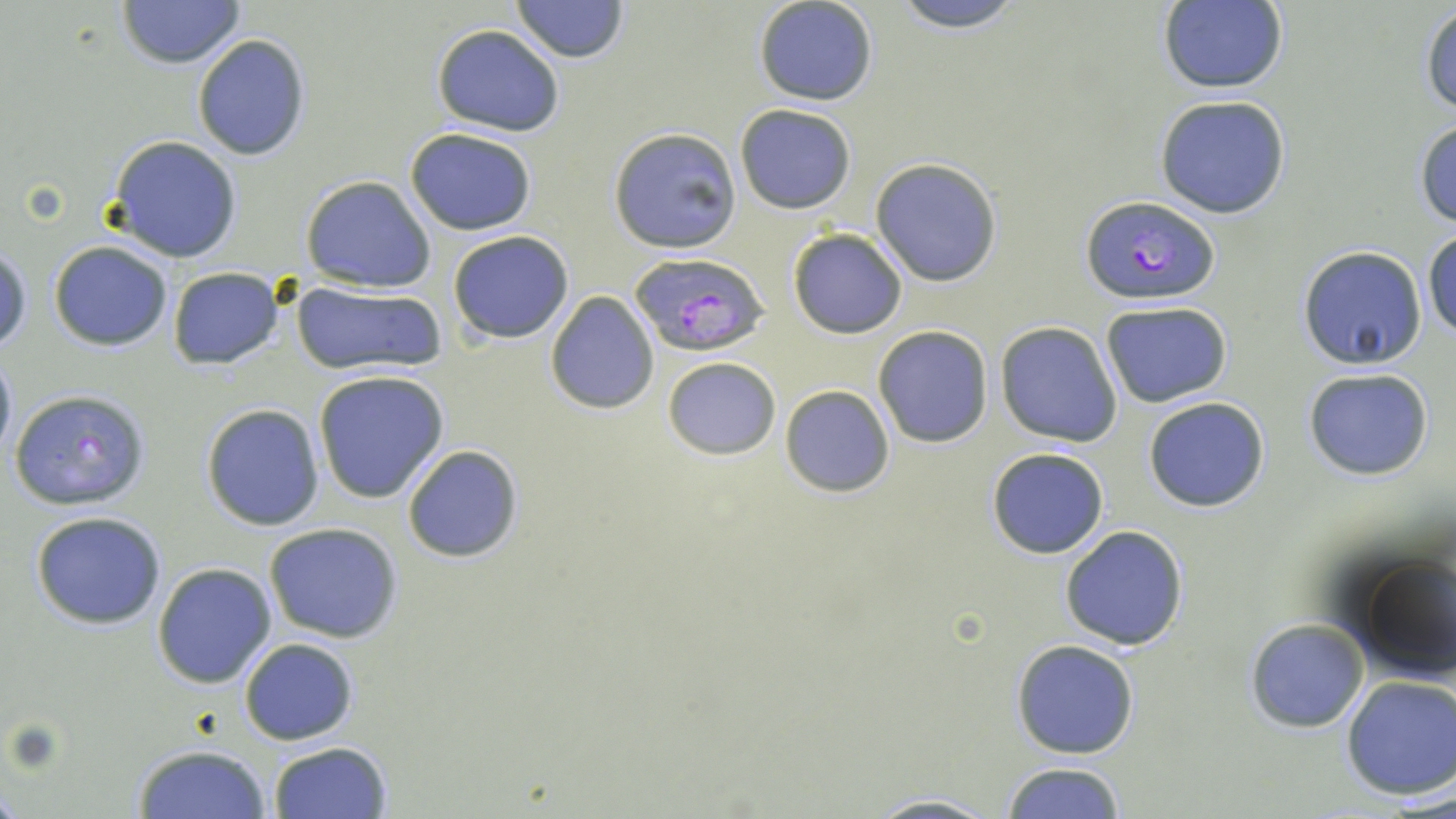
Summary:
  - Coordinate format: approximate bounding boxes as (x1, y1, x2, y2) in pixels
  - Uninfected red blood cell locations: (116, 0, 245, 69), (887, 0, 1027, 33), (513, 1, 629, 61), (754, 1, 878, 105), (1156, 1, 1288, 93), (1420, 5, 1456, 116), (431, 24, 564, 136), (192, 34, 310, 161), (1155, 95, 1291, 218), (735, 103, 856, 214), (1414, 117, 1456, 229), (608, 127, 741, 252), (405, 128, 538, 236), (107, 136, 242, 263), (869, 159, 1002, 287), (300, 176, 438, 293), (787, 228, 907, 338), (448, 231, 575, 344), (1424, 231, 1456, 341), (1, 240, 32, 356), (48, 240, 174, 351), (1298, 244, 1428, 369), (167, 267, 285, 369), (291, 280, 448, 377), (545, 290, 660, 416), (1099, 300, 1233, 408), (996, 321, 1123, 447), (873, 325, 994, 448), (0, 345, 16, 464), (662, 356, 780, 459), (1302, 367, 1434, 480), (314, 370, 451, 504), (780, 384, 895, 498), (1143, 396, 1271, 513), (201, 403, 325, 531), (402, 444, 523, 564), (986, 447, 1110, 559), (29, 510, 168, 629), (263, 523, 405, 644), (1059, 525, 1188, 650), (1348, 551, 1456, 686), (152, 563, 277, 688), (1244, 619, 1369, 734), (240, 637, 358, 745), (1010, 640, 1139, 759), (1341, 675, 1456, 800), (268, 741, 394, 819), (132, 744, 273, 819), (1001, 761, 1128, 818), (861, 793, 1006, 819)
  - Plasmodium falciparum-infected red blood cell locations: (1078, 194, 1219, 306), (627, 253, 771, 356), (8, 387, 152, 512)
  - Slide-level diagnosis: Plasmodium falciparum
  - Field of view: one of a larger specimen
  - Preparation: thin blood smear
  - Magnification: 1000x
  - Modality: light microscopy
  - Stain: May-Grünwald-Giemsa
  - Image size: 1456×819 pixels